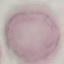

Summary:
  - Result: no malaria parasites seen
  - Preparation: thin blood film
  - Image type: automatically extracted cell patch, resized to 64 × 64 pixels
  - Stain: Giemsa
  - Capture: smartphone through the microscope eyepiece